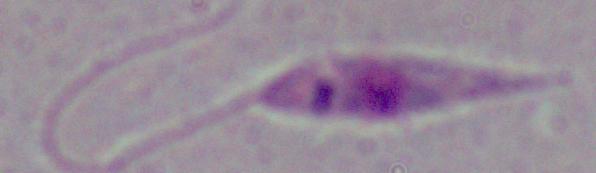

1000x magnification. A Leishmania parasite is seen. Micrograph.